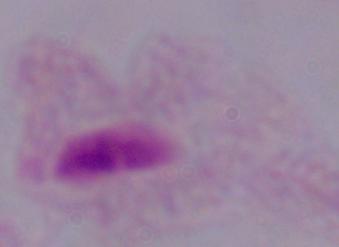

identification = trichomonad
modality = micrograph
magnification = 1000x